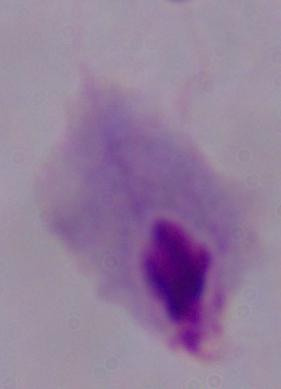
magnification: 1000x
identification: trichomonad
modality: micrograph